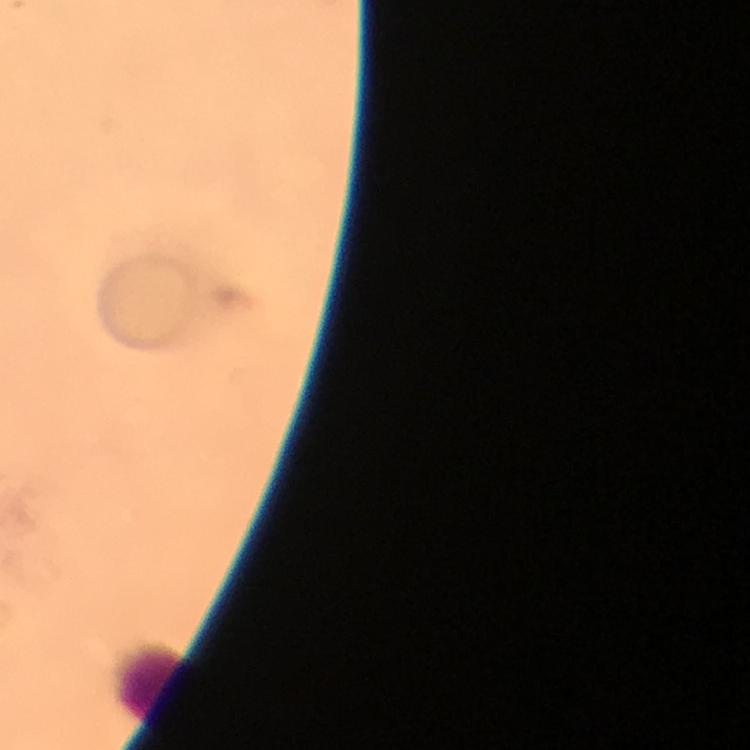 Approximate object centers, in pixels from the top-left corner. Leukocyte locations: (x=151, y=680). Cropped region of a single field of view. From a malaria diagnostic workup. Immersion oil applied. Giemsa stain. Thick blood film. 100x magnification. Image is 750×750 pixels. Plasmodium parasites: none detected. Smartphone photograph taken through a microscope.